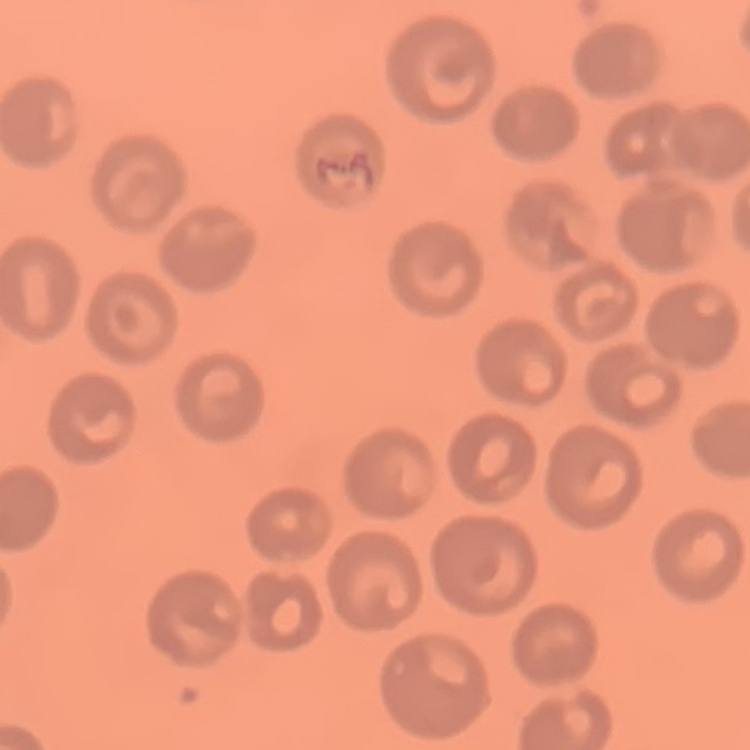

{
  "red_blood_cell_morphology": "no rouleaux formation",
  "preparation": "thin blood film",
  "stain": "Field's or Giemsa",
  "image_type": "one tile cut from a larger photomicrograph"
}